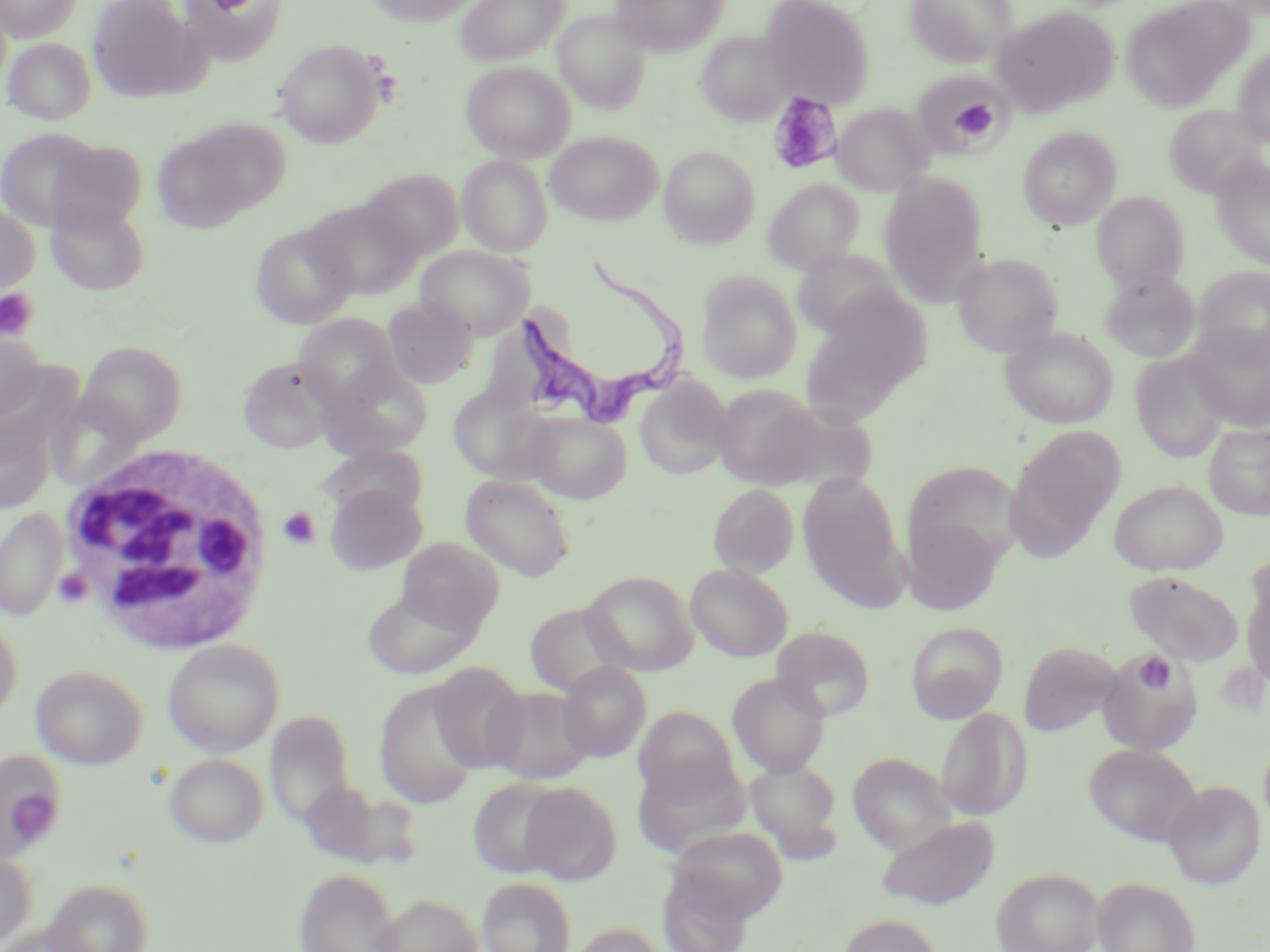
Approximate bounding boxes as (x1, y1, x2, y2) in pixels. Uninfected red blood cell locations: (0, 0, 83, 42), (88, 0, 199, 102), (180, 0, 288, 64), (364, 0, 480, 26), (455, 0, 570, 66), (610, 0, 728, 56), (760, 0, 874, 107), (903, 0, 1017, 67), (1120, 0, 1251, 112), (991, 5, 1118, 118), (554, 9, 651, 113), (696, 31, 792, 126), (2, 37, 97, 125), (274, 39, 386, 148), (1232, 48, 1270, 147), (461, 61, 576, 162), (911, 70, 1012, 157), (832, 102, 934, 195), (1164, 105, 1267, 199), (155, 118, 288, 231), (0, 127, 106, 231), (1017, 127, 1121, 230), (545, 131, 663, 225), (46, 139, 147, 234), (659, 146, 760, 248), (458, 155, 552, 257), (1210, 155, 1270, 271), (362, 169, 464, 261), (879, 175, 988, 302), (763, 179, 864, 274), (1092, 192, 1189, 292), (306, 197, 422, 299), (46, 199, 151, 296), (0, 202, 39, 298), (249, 222, 357, 330), (417, 245, 534, 339), (793, 249, 903, 339), (952, 252, 1063, 356), (1193, 265, 1270, 366), (1099, 270, 1201, 363), (696, 271, 802, 384), (805, 290, 930, 415), (382, 298, 477, 388), (294, 314, 404, 412), (1186, 325, 1270, 433), (1001, 326, 1118, 429), (0, 329, 48, 423), (78, 341, 187, 444), (1130, 352, 1233, 462), (237, 357, 335, 454), (319, 364, 434, 459), (635, 376, 733, 480), (712, 385, 826, 489), (448, 386, 556, 485), (762, 402, 879, 493), (0, 409, 56, 514), (525, 411, 631, 503), (1204, 423, 1270, 520), (1005, 426, 1125, 559), (319, 444, 428, 520), (901, 461, 1023, 570), (796, 473, 909, 610), (460, 475, 575, 581), (1109, 480, 1227, 576), (325, 482, 426, 575), (708, 484, 799, 577), (0, 509, 70, 622), (900, 516, 1005, 615), (397, 536, 504, 634), (1240, 558, 1270, 689), (685, 564, 792, 661), (1124, 570, 1244, 666), (581, 571, 697, 676), (362, 586, 480, 681), (524, 602, 628, 698), (0, 613, 23, 724), (906, 622, 1008, 723), (772, 626, 874, 720), (163, 638, 285, 757), (1018, 641, 1123, 737), (1098, 650, 1202, 754), (429, 661, 529, 773), (558, 661, 651, 762), (31, 664, 148, 770), (728, 672, 830, 777), (374, 679, 482, 809), (483, 686, 594, 784), (633, 707, 740, 802), (937, 707, 1032, 821), (265, 709, 357, 826), (1084, 744, 1202, 846), (0, 751, 66, 859), (164, 753, 268, 848), (847, 753, 955, 854), (633, 757, 750, 858), (746, 759, 842, 861), (299, 778, 398, 867), (468, 778, 566, 878), (1164, 780, 1266, 890), (518, 781, 622, 884), (875, 815, 1000, 911), (669, 825, 789, 922), (0, 849, 38, 949), (294, 868, 401, 952), (991, 868, 1103, 952), (657, 870, 756, 952), (476, 876, 576, 952), (1092, 877, 1201, 952), (42, 878, 154, 952), (372, 893, 483, 952), (838, 914, 943, 952), (567, 923, 668, 952), (3, 924, 99, 952). Trypanosoma brucei locations: (503, 255, 693, 421). Platelet locations: (766, 92, 841, 176), (946, 96, 998, 141), (0, 288, 39, 343), (277, 506, 321, 551), (54, 568, 93, 607), (1133, 652, 1177, 695), (3, 775, 61, 846). White blood cell locations: (59, 439, 276, 654). Slide-level diagnosis: Trypanosoma brucei. Light microscopy. Image is 1270×952 pixels. Captured at 1000x magnification. Thin blood film. May-Grünwald-Giemsa-stained preparation. Single field of view.